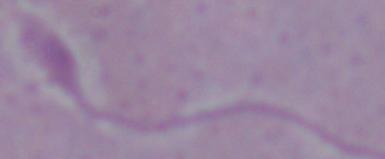
modality = photomicrograph
identification = Leishmania
magnification = 1000x